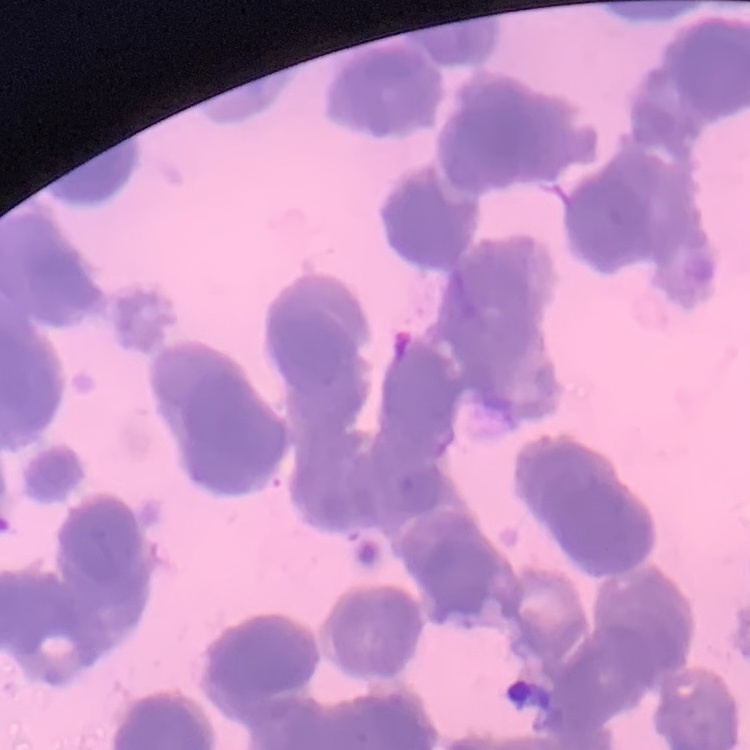
erythrocyte morphology = rouleaux formation
preparation = thin blood smear
image type = square crop of a larger photomicrograph
stain = Field's or Giemsa